Classify this cell by malaria status.
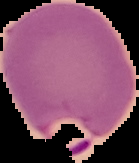
Parasitized.

image size = 139×163 pixels
preparation = thin blood smear
image type = cell region segmented out of the field of view; surrounding area masked to black